Outline each blood parasite and name the species.
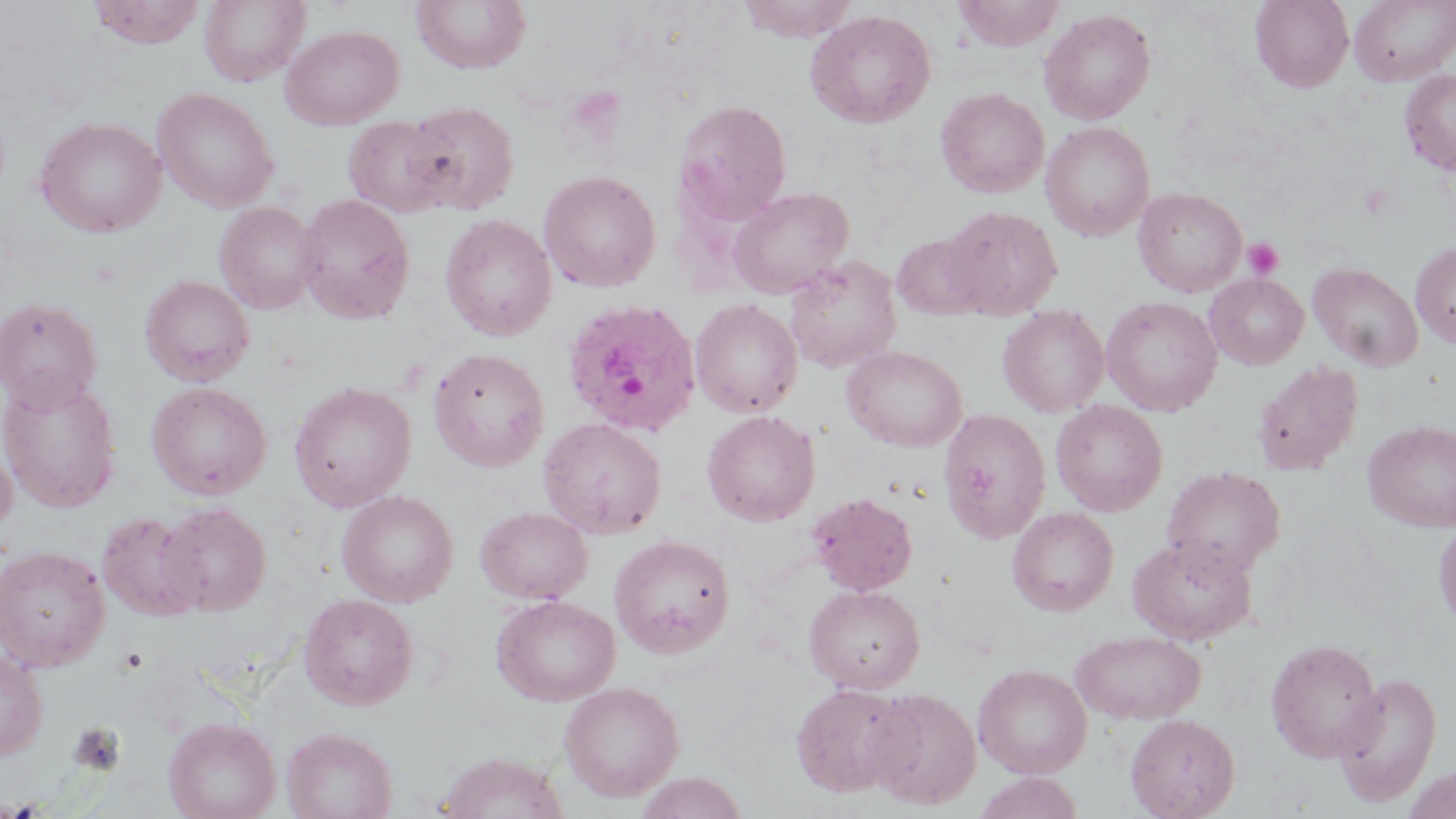
Approximate bounding boxes as (x1,y1)-(x2,y2) corner pairs in pixels.
Plasmodium ovale-infected red blood cells: (561,297)-(703,438).
No Plasmodium falciparum, Plasmodium malariae, Plasmodium vivax, Babesia divergens, or Trypanosoma brucei observed.

Uninfected red blood cell locations: (88,0)-(206,48), (199,0)-(308,86), (411,0)-(532,73), (736,0)-(862,41), (952,0)-(1066,50), (1250,0)-(1353,92), (1350,0)-(1456,86), (1039,8)-(1156,125), (805,9)-(936,127), (281,24)-(404,130), (1399,68)-(1456,176), (152,87)-(279,213), (935,87)-(1050,198), (674,99)-(791,225), (401,100)-(520,214), (36,116)-(166,237), (343,116)-(453,218), (1040,121)-(1155,241), (538,169)-(661,291), (727,187)-(854,300), (1133,187)-(1247,296), (294,194)-(415,324), (214,201)-(323,315), (941,205)-(1062,319), (440,214)-(557,341), (892,232)-(989,320), (1411,241)-(1456,348), (784,254)-(901,374), (1309,263)-(1424,372), (1205,273)-(1309,369), (140,274)-(254,387), (1,296)-(103,410), (1101,296)-(1222,416), (690,298)-(802,418), (998,305)-(1110,417), (842,345)-(968,452), (428,347)-(549,472), (1252,361)-(1364,475), (0,373)-(123,513), (147,381)-(271,499), (289,381)-(417,512), (1050,400)-(1168,516), (939,405)-(1165,527), (701,409)-(820,526), (938,409)-(1050,543), (538,417)-(667,539), (1363,419)-(1456,531), (0,437)-(17,540), (1161,466)-(1285,578), (336,490)-(458,607), (808,492)-(918,596), (158,502)-(270,615), (476,506)-(593,604), (1007,506)-(1118,616), (97,511)-(208,621), (1433,519)-(1456,633), (609,534)-(735,658), (1128,534)-(1257,645), (0,545)-(110,671), (803,585)-(925,694), (298,593)-(418,710), (491,594)-(621,706), (1072,629)-(1206,724), (1265,638)-(1384,762), (0,648)-(50,761), (973,664)-(1091,779), (1334,671)-(1443,806), (558,681)-(685,802), (790,683)-(911,797), (865,688)-(981,810), (1125,713)-(1240,819), (164,717)-(281,819), (281,727)-(397,819), (435,751)-(569,819), (1402,763)-(1456,819), (635,772)-(748,818), (973,772)-(1084,819). Platelet locations: (1359,183)-(1394,219), (1243,237)-(1285,280), (69,723)-(126,775). Slide-level diagnosis: Plasmodium ovale. Thin blood smear. Optical microscopy. Image is 1456×819 pixels. May-Grünwald-Giemsa-stained preparation. Single field of view. 1000x magnification.